Point out each Plasmodium parasite.
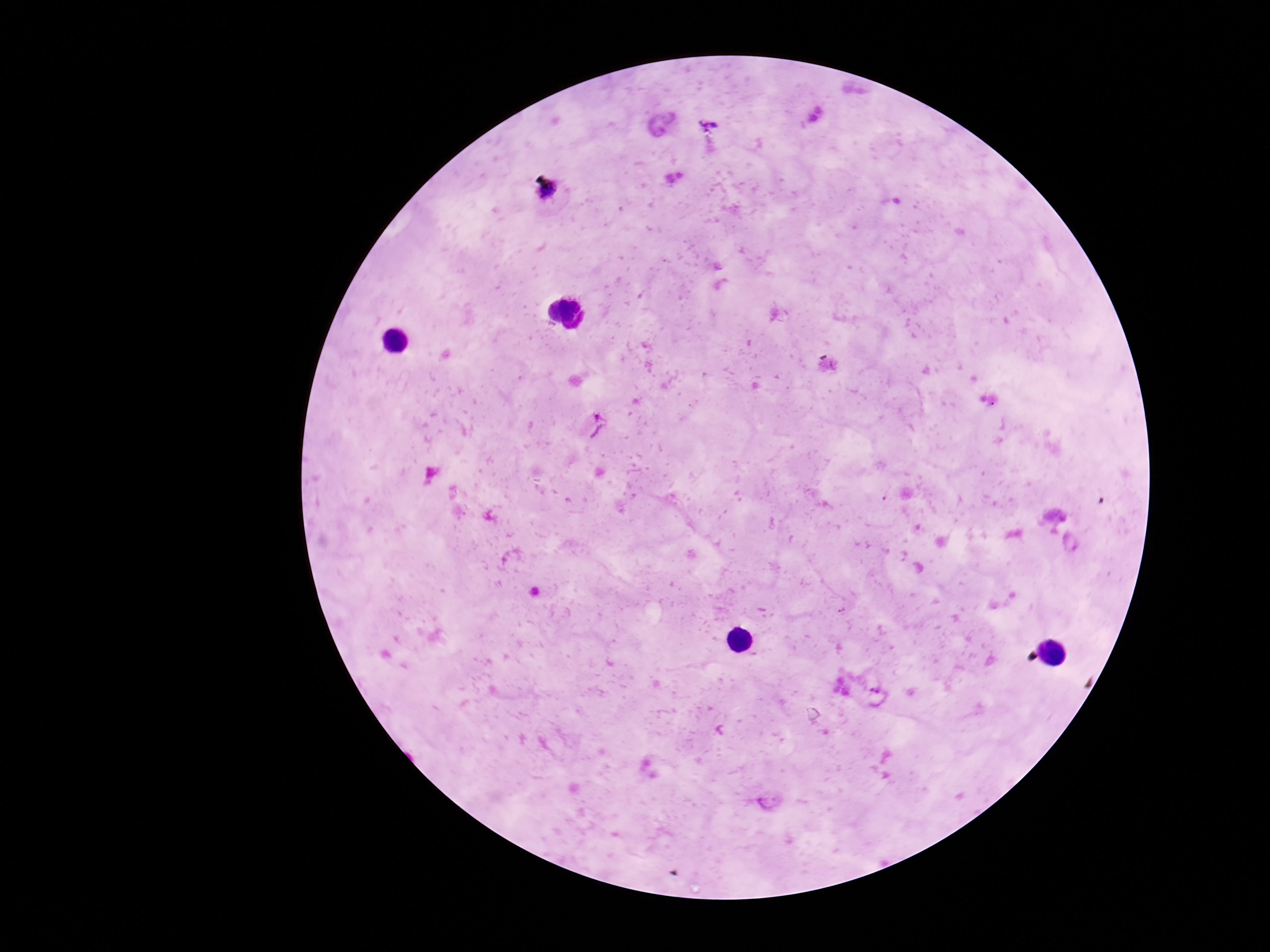

Approximate centers as {x, y} in pixels.
Plasmodium parasites: {709, 123}, {661, 124}, {549, 193}, {598, 425}, {1073, 542}, {872, 687}, {769, 800}.

{
  "field_of_view": "one from this slide",
  "image_size": "1270×952 pixels",
  "magnification": "100x",
  "stain": "Giemsa",
  "preparation": "thick peripheral-blood smear",
  "patient_malaria_status": "infected",
  "capture": "smartphone camera through the microscope eyepiece"
}